Describe the morphology of the red blood cells.
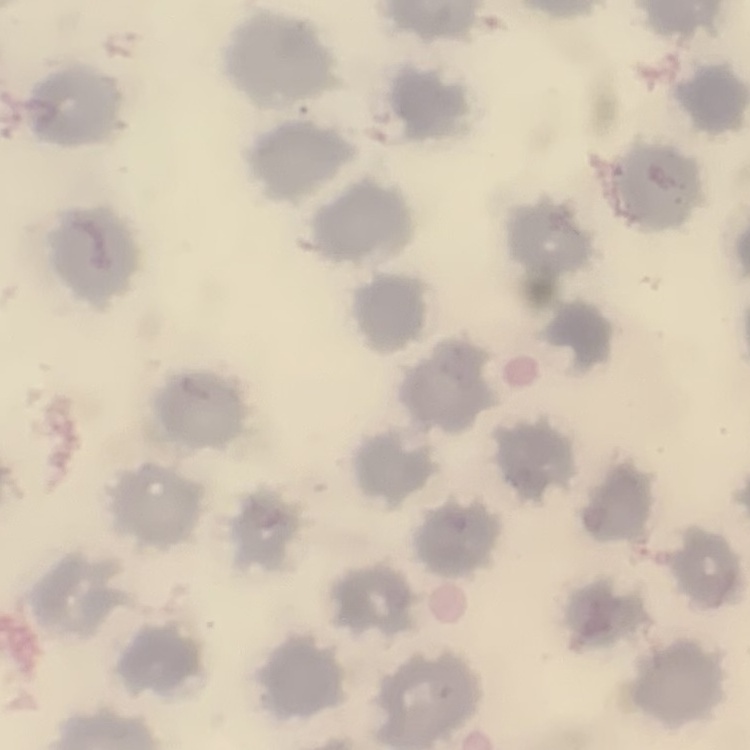
They show no rouleaux formation.

Square crop of a larger photomicrograph. Thin blood film. Field's or Giemsa stain.